Assess for malaria.
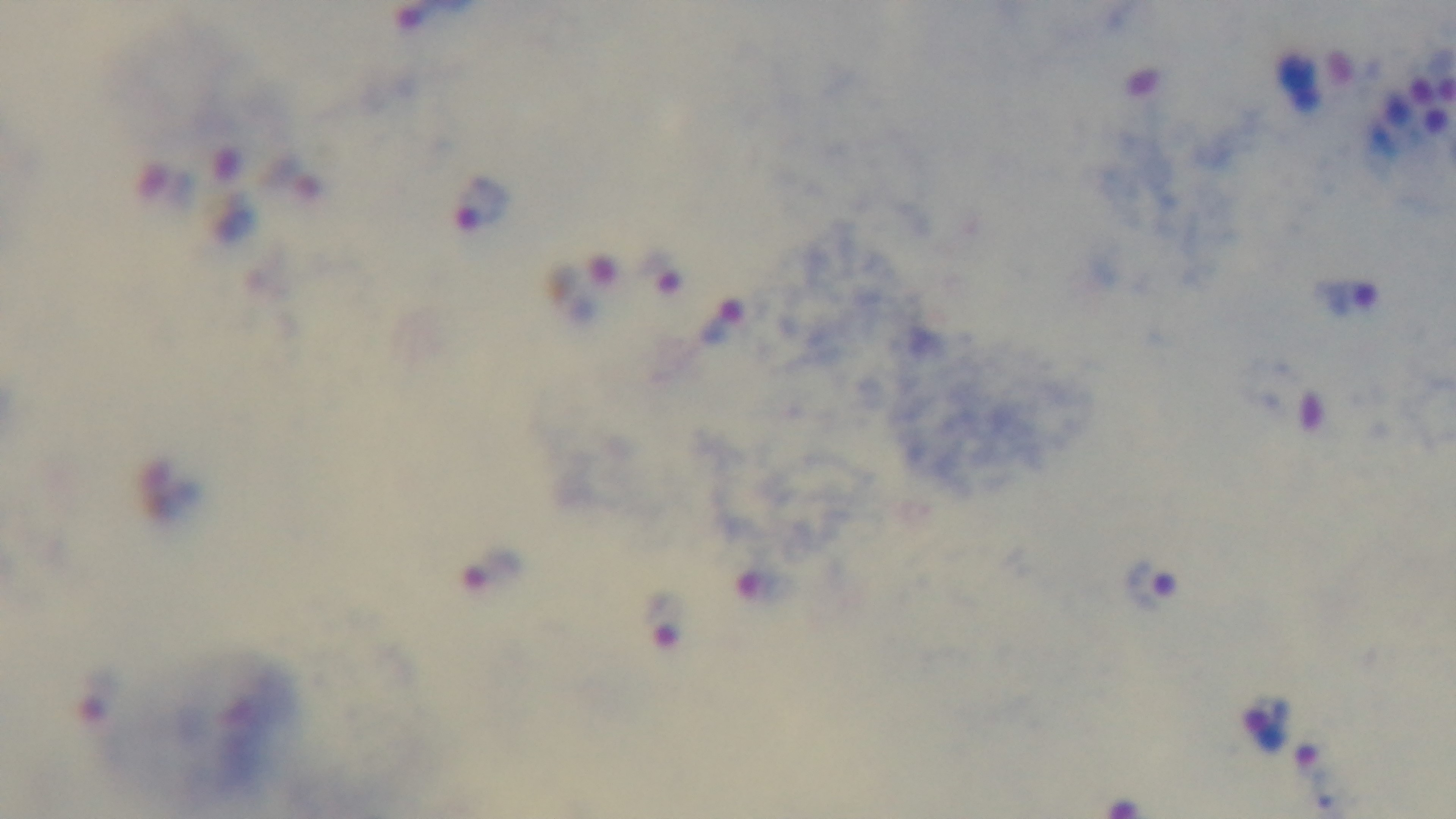
Infected.

Summary:
  - Field of view: single
  - Capture: mounted 4K digital camera
  - Modality: light microscopy
  - Stain: Giemsa
  - Objective: 100x oil immersion
  - Preparation: thick